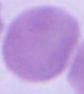

Summary:
  - Magnification: 1000x
  - Identification: red blood cell
  - Modality: photomicrograph